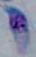
Toxoplasma gondii is seen. 1000x magnification. Photomicrograph.